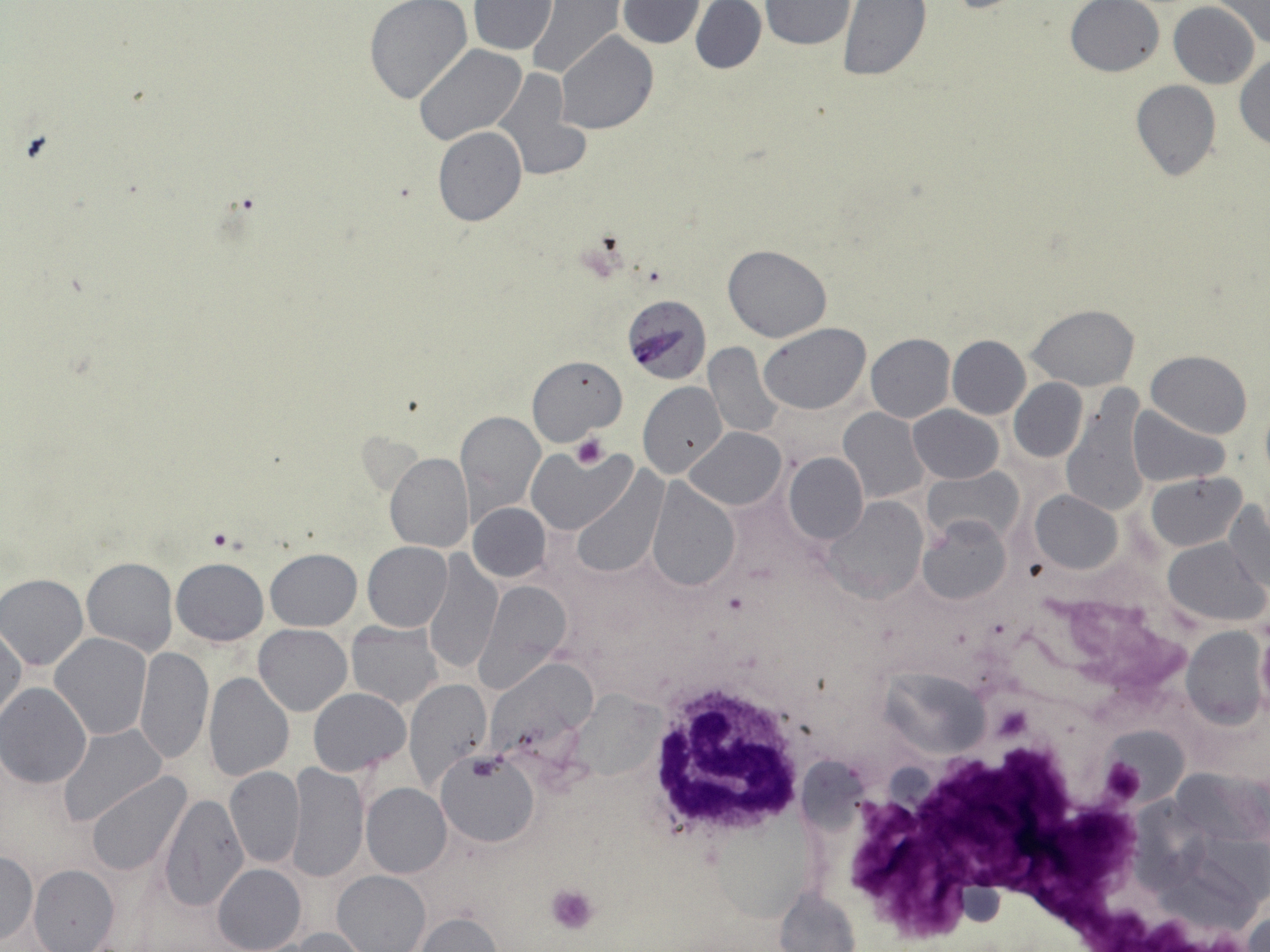

Summary:
  - Coordinate format: approximate bounding boxes as named x1/y1/x2/y2 corners in pixels
  - Uninfected red blood cell locations: (x1=526, y1=0, x2=626, y2=81), (x1=626, y1=0, x2=769, y2=57), (x1=1213, y1=0, x2=1270, y2=49), (x1=468, y1=1, x2=557, y2=54), (x1=618, y1=1, x2=704, y2=47), (x1=690, y1=1, x2=766, y2=75), (x1=759, y1=1, x2=858, y2=51), (x1=836, y1=1, x2=931, y2=82), (x1=1065, y1=1, x2=1164, y2=77), (x1=363, y1=2, x2=471, y2=102), (x1=1169, y1=2, x2=1260, y2=89), (x1=556, y1=32, x2=657, y2=134), (x1=413, y1=44, x2=527, y2=145), (x1=1234, y1=55, x2=1270, y2=151), (x1=495, y1=68, x2=584, y2=181), (x1=1130, y1=79, x2=1221, y2=181), (x1=433, y1=126, x2=526, y2=226), (x1=723, y1=244, x2=832, y2=342), (x1=1028, y1=304, x2=1140, y2=391), (x1=760, y1=323, x2=872, y2=415), (x1=865, y1=333, x2=954, y2=423), (x1=946, y1=335, x2=1030, y2=419), (x1=703, y1=341, x2=785, y2=439), (x1=1146, y1=349, x2=1253, y2=438), (x1=526, y1=355, x2=626, y2=444), (x1=1009, y1=379, x2=1088, y2=461), (x1=639, y1=382, x2=727, y2=478), (x1=1060, y1=391, x2=1152, y2=518), (x1=909, y1=405, x2=1002, y2=483), (x1=1127, y1=405, x2=1231, y2=486), (x1=839, y1=407, x2=930, y2=502), (x1=454, y1=410, x2=544, y2=519), (x1=687, y1=427, x2=785, y2=510), (x1=527, y1=445, x2=633, y2=534), (x1=784, y1=451, x2=867, y2=543), (x1=385, y1=453, x2=474, y2=553), (x1=924, y1=467, x2=1023, y2=547), (x1=568, y1=469, x2=666, y2=578), (x1=1147, y1=472, x2=1245, y2=550), (x1=645, y1=478, x2=739, y2=591), (x1=1030, y1=491, x2=1122, y2=574), (x1=824, y1=497, x2=927, y2=600), (x1=1225, y1=501, x2=1270, y2=591), (x1=468, y1=502, x2=552, y2=581), (x1=920, y1=513, x2=1012, y2=603), (x1=1162, y1=537, x2=1268, y2=626), (x1=362, y1=541, x2=453, y2=631), (x1=265, y1=549, x2=361, y2=630), (x1=422, y1=550, x2=503, y2=676), (x1=82, y1=557, x2=178, y2=656), (x1=171, y1=557, x2=268, y2=645), (x1=1, y1=574, x2=89, y2=670), (x1=476, y1=579, x2=571, y2=690), (x1=346, y1=624, x2=442, y2=708), (x1=253, y1=625, x2=352, y2=716), (x1=0, y1=626, x2=25, y2=727), (x1=1256, y1=626, x2=1270, y2=713), (x1=1182, y1=627, x2=1268, y2=730), (x1=50, y1=634, x2=151, y2=740), (x1=134, y1=646, x2=212, y2=765), (x1=487, y1=657, x2=595, y2=755), (x1=880, y1=671, x2=993, y2=758), (x1=204, y1=672, x2=294, y2=781), (x1=404, y1=679, x2=492, y2=790), (x1=0, y1=684, x2=91, y2=788), (x1=309, y1=688, x2=410, y2=775), (x1=573, y1=695, x2=673, y2=781), (x1=58, y1=724, x2=168, y2=827), (x1=1107, y1=725, x2=1189, y2=804), (x1=437, y1=752, x2=538, y2=847), (x1=287, y1=763, x2=368, y2=883), (x1=225, y1=767, x2=304, y2=869), (x1=1170, y1=768, x2=1267, y2=848), (x1=86, y1=772, x2=191, y2=875), (x1=362, y1=784, x2=452, y2=878), (x1=159, y1=793, x2=247, y2=913), (x1=1, y1=851, x2=38, y2=944), (x1=28, y1=864, x2=119, y2=952), (x1=213, y1=864, x2=305, y2=952), (x1=332, y1=870, x2=430, y2=952), (x1=952, y1=879, x2=1009, y2=926), (x1=773, y1=886, x2=861, y2=952), (x1=1243, y1=911, x2=1269, y2=951), (x1=414, y1=912, x2=502, y2=951), (x1=279, y1=927, x2=373, y2=951)
  - Platelet locations: (x1=571, y1=434, x2=609, y2=469), (x1=1097, y1=758, x2=1147, y2=807), (x1=546, y1=884, x2=599, y2=934)
  - White blood cell locations: (x1=639, y1=672, x2=814, y2=853)
  - Plasmodium falciparum-infected red blood cell locations: (x1=621, y1=294, x2=711, y2=385)
  - Slide-level diagnosis: Plasmodium falciparum
  - Modality: optical microscopy
  - Stain: May-Grünwald-Giemsa
  - Field of view: one of a larger specimen
  - Magnification: 1000x
  - Preparation: thin blood film
  - Image size: 1270×952 pixels